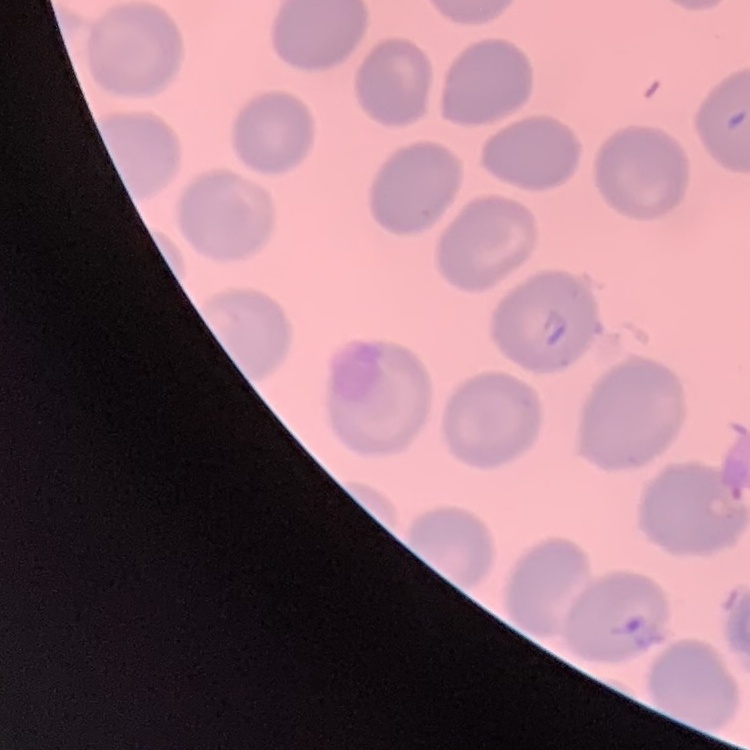

The red blood cells exhibit no rouleaux formation. One tile cut from a larger photomicrograph. Thin peripheral smear. Stained with either Field's or Giemsa.